Report the malaria status of this cell.
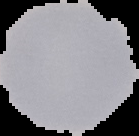

It is uninfected.

preparation = thin blood film
image size = 139×136 pixels
image type = segmented cell region on a black background